Assess this cell for malaria.
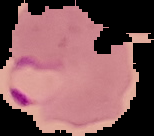
Parasitized.

From a thin blood film. The area outside the segmented cell region is set to black. Image is 154×136 pixels.